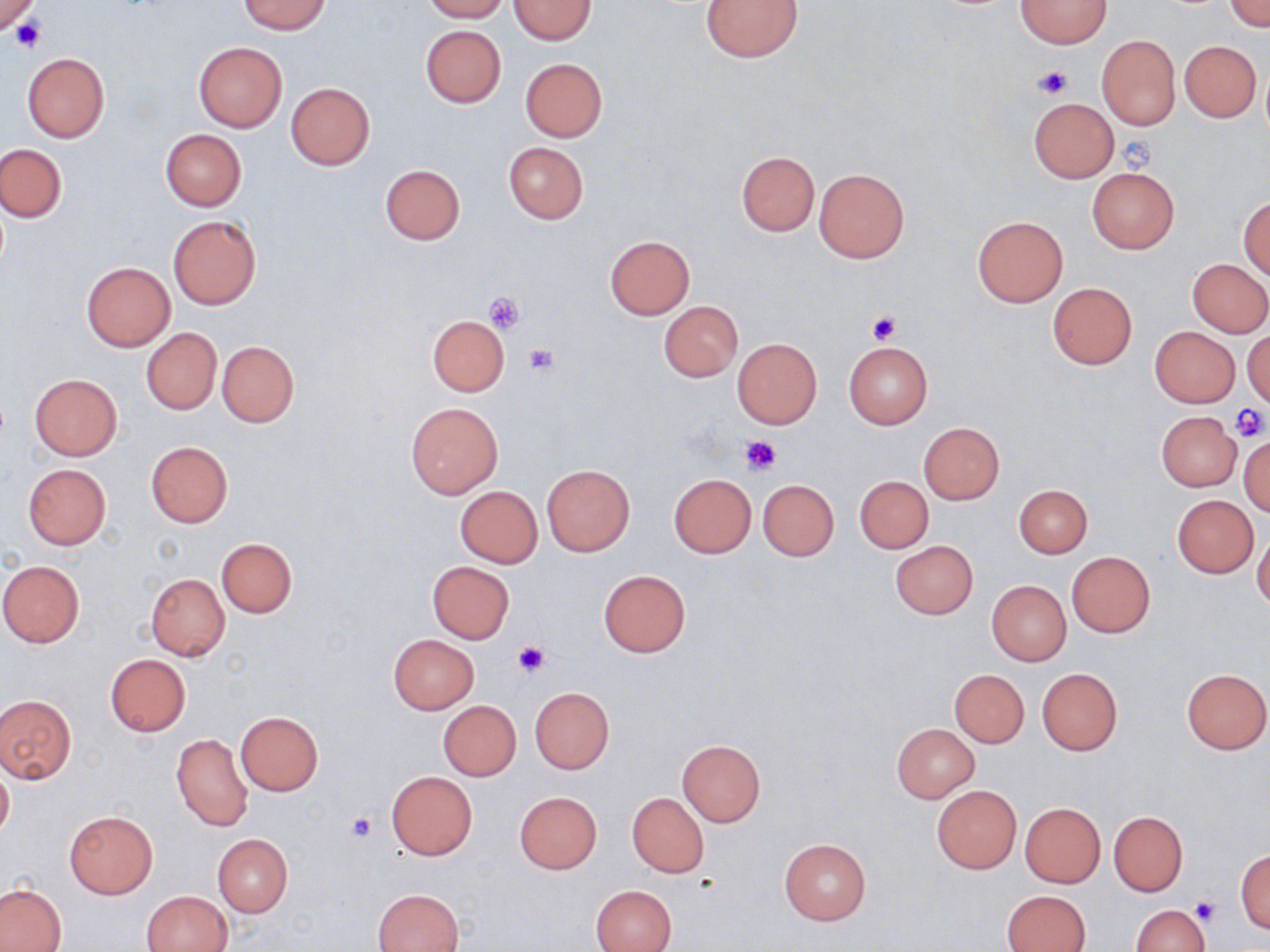

slide-level diagnosis = negative for blood parasites
uninfected red blood cell locations = approximate bounding boxes as [x1, y1, x2, y2] in pixels: [240, 0, 329, 35], [420, 0, 509, 22], [508, 0, 597, 45], [700, 0, 804, 63], [1015, 0, 1110, 48], [0, 1, 42, 36], [1226, 1, 1269, 33], [420, 25, 506, 106], [1097, 35, 1180, 130], [1180, 41, 1261, 121], [193, 42, 287, 132], [22, 53, 109, 142], [520, 57, 607, 141], [286, 83, 375, 169], [1028, 98, 1118, 181], [160, 129, 247, 211], [503, 141, 588, 224], [0, 144, 67, 223], [736, 151, 819, 235], [380, 164, 466, 245], [1086, 167, 1179, 254], [813, 168, 910, 263], [1238, 195, 1269, 278], [167, 215, 261, 309], [972, 216, 1068, 306], [604, 235, 694, 319], [1188, 259, 1270, 337], [82, 263, 174, 350], [1046, 282, 1138, 369], [659, 301, 742, 381], [427, 314, 510, 396], [1149, 326, 1239, 406], [141, 328, 221, 414], [1244, 329, 1270, 408], [733, 338, 821, 428], [218, 341, 298, 427], [843, 341, 932, 428], [30, 374, 122, 459], [406, 402, 503, 498], [1156, 411, 1242, 490], [918, 422, 1005, 504], [1239, 437, 1270, 515], [145, 441, 234, 527], [23, 464, 110, 549], [542, 464, 634, 555], [668, 474, 755, 559], [854, 475, 933, 553], [758, 479, 839, 561], [1014, 484, 1091, 558], [455, 486, 542, 567], [1172, 496, 1258, 577], [1253, 532, 1270, 613], [217, 538, 296, 617], [889, 540, 978, 619], [1067, 552, 1154, 637], [0, 560, 85, 647], [426, 561, 516, 644], [598, 569, 691, 657], [146, 573, 230, 659], [987, 580, 1071, 666], [388, 634, 479, 713], [105, 654, 191, 737], [1182, 668, 1269, 754], [949, 669, 1029, 748], [1037, 669, 1122, 755], [530, 687, 614, 772], [1, 694, 76, 783], [438, 700, 521, 781], [235, 712, 322, 796], [892, 723, 978, 802], [904, 731, 991, 851], [171, 733, 254, 832], [676, 740, 764, 827], [0, 764, 13, 842], [386, 771, 477, 860], [932, 786, 1021, 873], [513, 791, 602, 873], [627, 792, 708, 878], [1020, 802, 1105, 887], [65, 811, 158, 899], [1107, 811, 1187, 896], [213, 834, 292, 917], [779, 839, 872, 925], [1235, 850, 1269, 933], [591, 884, 677, 952], [0, 885, 67, 951], [373, 888, 463, 952], [141, 890, 233, 952], [1003, 890, 1091, 952], [1130, 904, 1210, 952]
magnification = 1000x
platelet locations = approximate bounding boxes as [x1, y1, x2, y2] in pixels: [0, 2, 42, 40], [10, 17, 48, 54], [1034, 66, 1072, 99], [1117, 136, 1157, 173], [483, 291, 525, 333], [866, 312, 901, 344], [523, 344, 557, 376], [1231, 403, 1268, 442], [739, 434, 782, 474], [512, 641, 549, 676], [346, 811, 378, 844], [1190, 896, 1221, 925]
field of view = one of a larger specimen
image size = 1270×952 pixels
preparation = thin blood smear
modality = light microscopy
stain = May-Grünwald-Giemsa